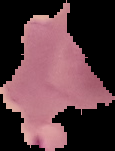
{
  "image_size": "115×151 pixels",
  "image_type": "cell region segmented out of the field of view; surrounding area masked to black",
  "result": "Plasmodium parasites detected",
  "preparation": "thin blood smear"
}